Identify the parasite.
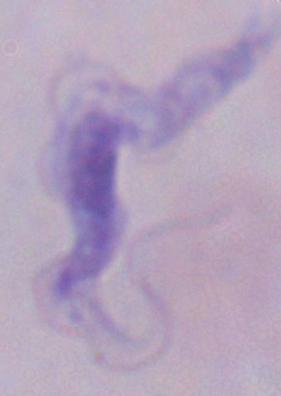
A trypanosome.

1000x magnification. Micrograph.